Give the position of every Plasmodium parasite visible.
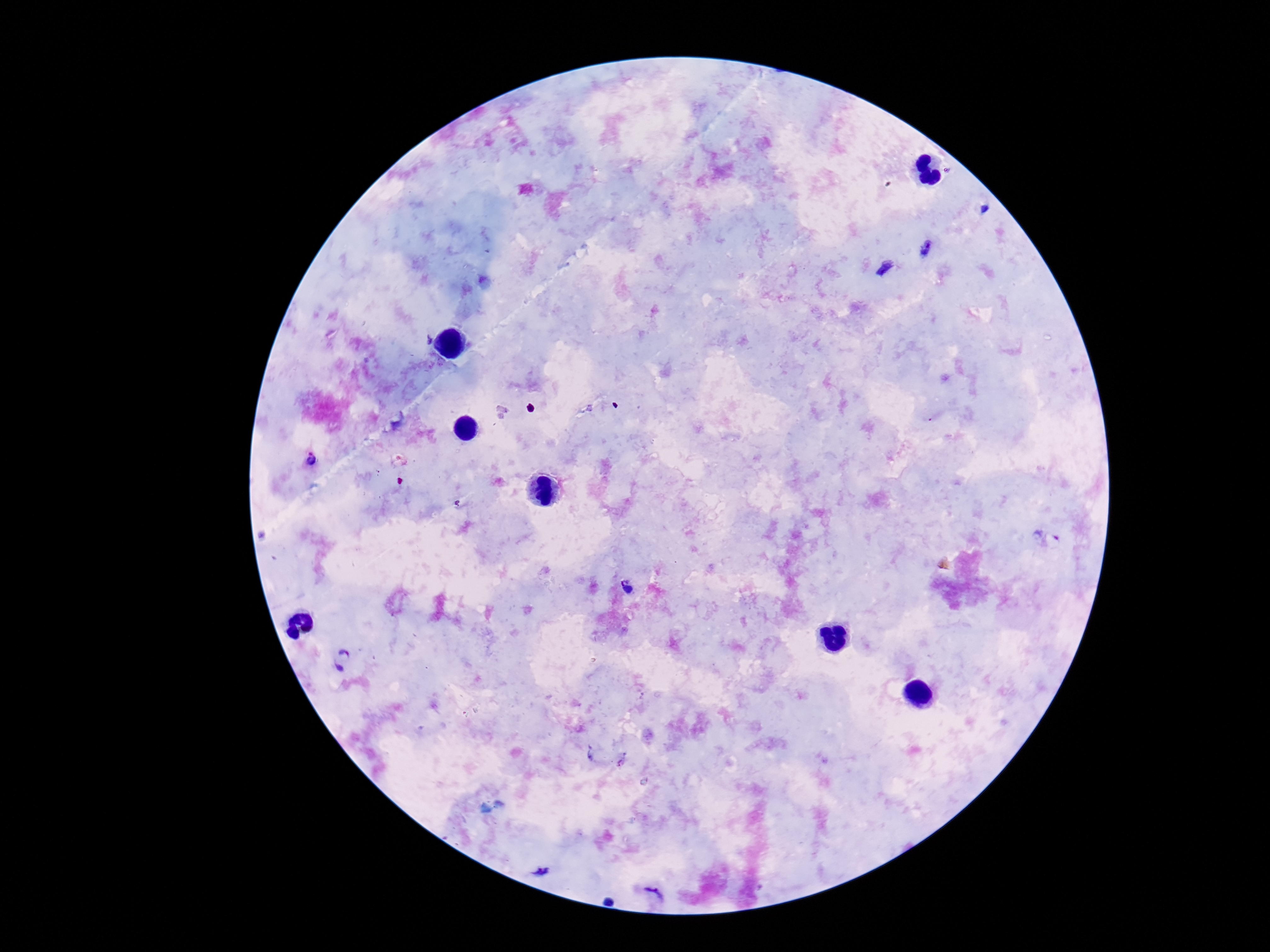

Approximate centers as [x, y] in pixels.
Plasmodium parasites: [925, 248], [884, 268], [312, 462], [1045, 538], [626, 586], [342, 658], [620, 759], [541, 870], [652, 895].

stain = Giemsa
field of view = single
image size = 1270×952 pixels
capture = smartphone camera through the microscope eyepiece
preparation = thick peripheral-blood smear
patient malaria status = infected
magnification = 100x